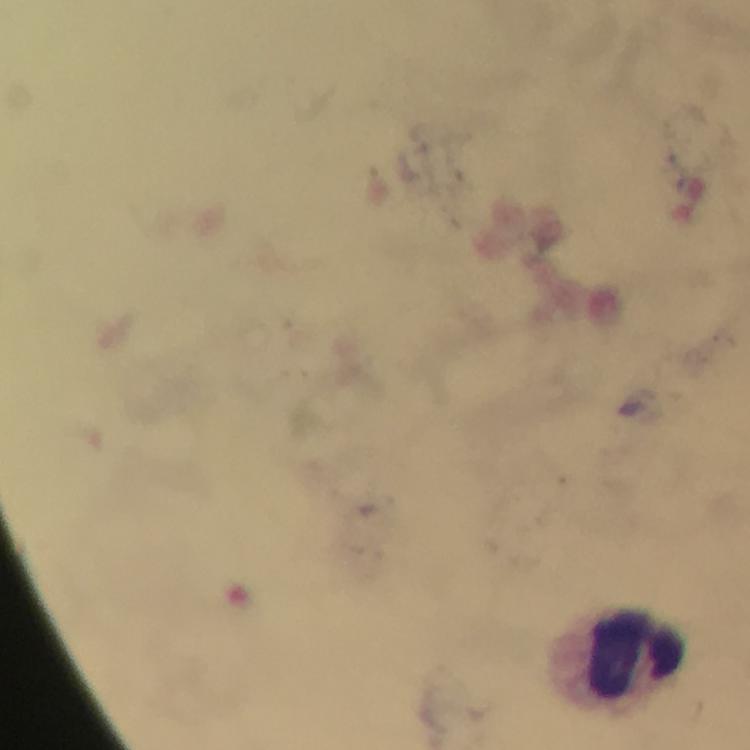
capture: smartphone photograph through a microscope
preparation: thick smear
magnification: 100x
cropped_from: a single field of view
immersion_oil: applied
leukocyte_locations: 'approximate object centers, in pixels from the top-left corner: (x=639, y=652)'
context: from a malaria diagnostic workup
image_size: 750×750 pixels
stain: Giemsa
malaria_parasites: none detected